Assess this cell for malaria.
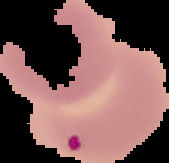
Parasitized.

From a thin blood smear. Segmented cell region on a black background. Image is 169×163 pixels.